Give the position of every Plasmodium parasite visible.
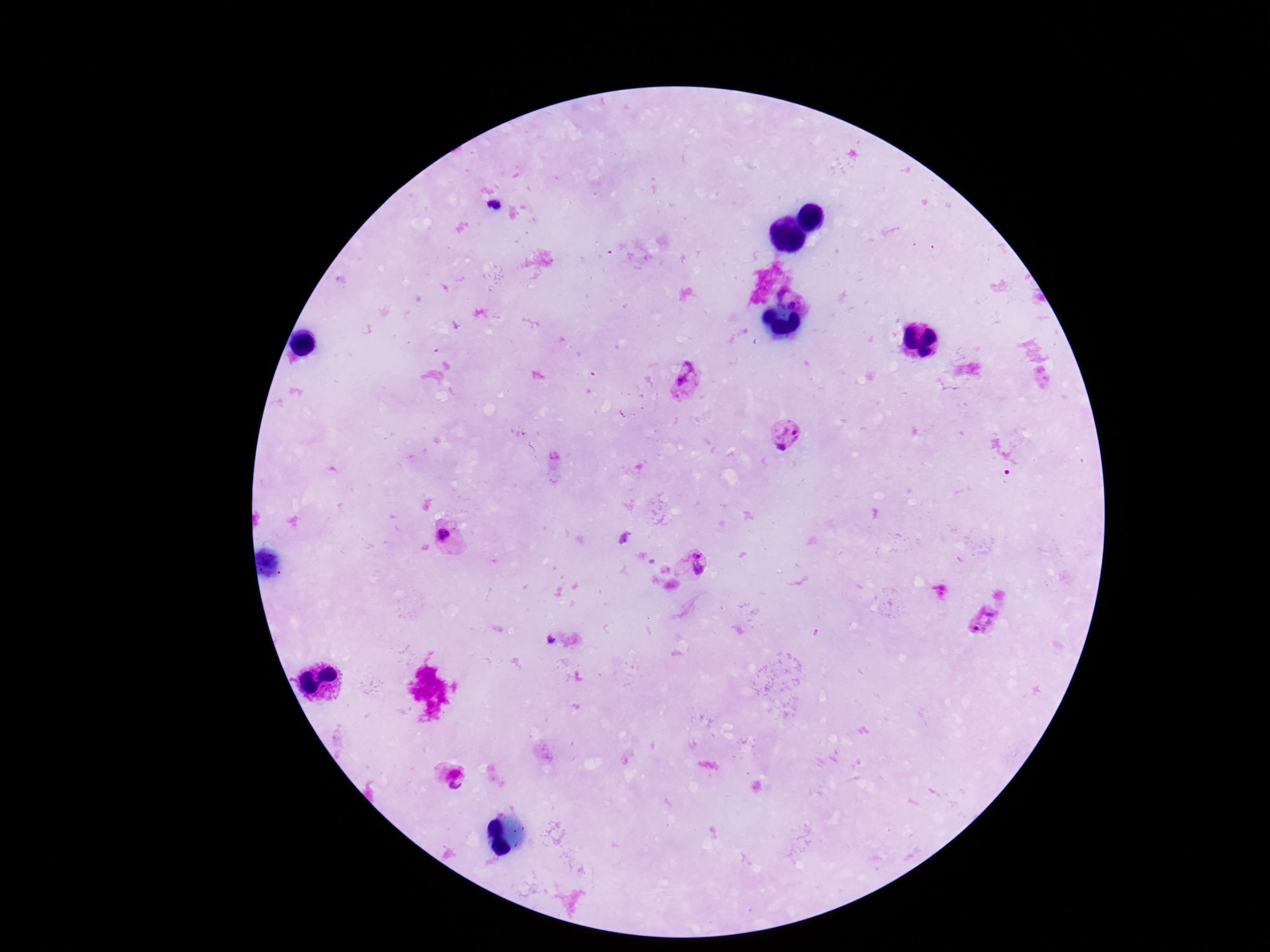

Approximate centers as [x, y] in pixels.
Plasmodium parasites: [689, 381], [787, 435], [446, 536], [694, 564], [987, 624], [452, 775].

Summary:
  - Image size: 1270×952 pixels
  - Magnification: 100x
  - Capture: smartphone camera through the microscope eyepiece
  - Preparation: thick blood film
  - Field of view: one from this slide
  - Stain: Giemsa
  - Patient malaria status: positive